Identify the parasite.
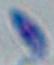
Toxoplasma gondii.

Summary:
  - Modality: micrograph
  - Magnification: 1000x